Comment on the morphology of the erythrocytes.
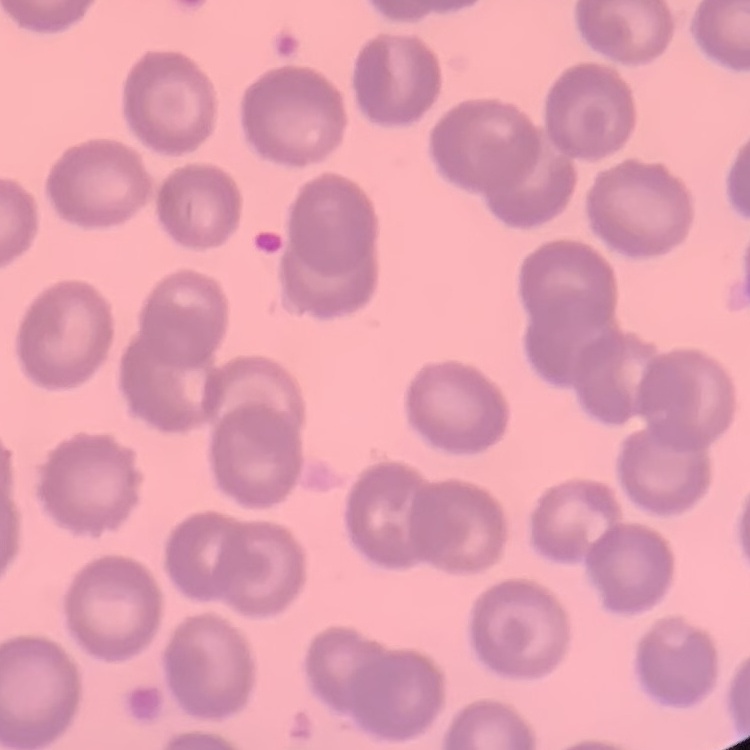

No rouleaux formation.

Summary:
  - Stain: Field's or Giemsa
  - Image type: square crop of a larger photomicrograph
  - Preparation: thin peripheral smear